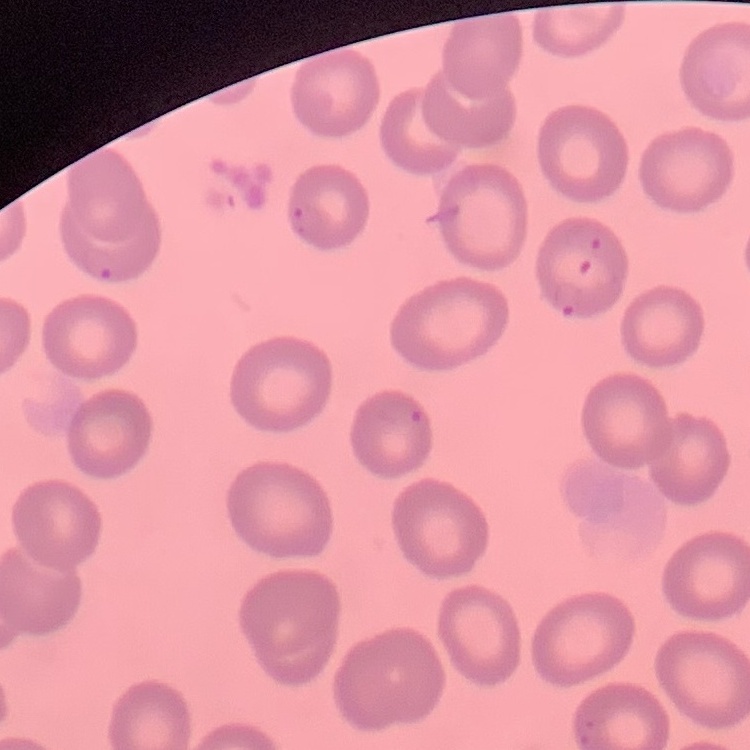

Summary:
  - Erythrocyte morphology: no rouleaux formation
  - Stain: Field's or Giemsa
  - Preparation: thin blood smear
  - Image type: one tile cut from a larger photomicrograph